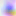

magnification = 400x
modality = photomicrograph
identification = Toxoplasma gondii